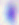 Toxoplasma gondii is seen. Captured at 400x magnification. Photomicrograph.